Locate every blood parasite and identify its species.
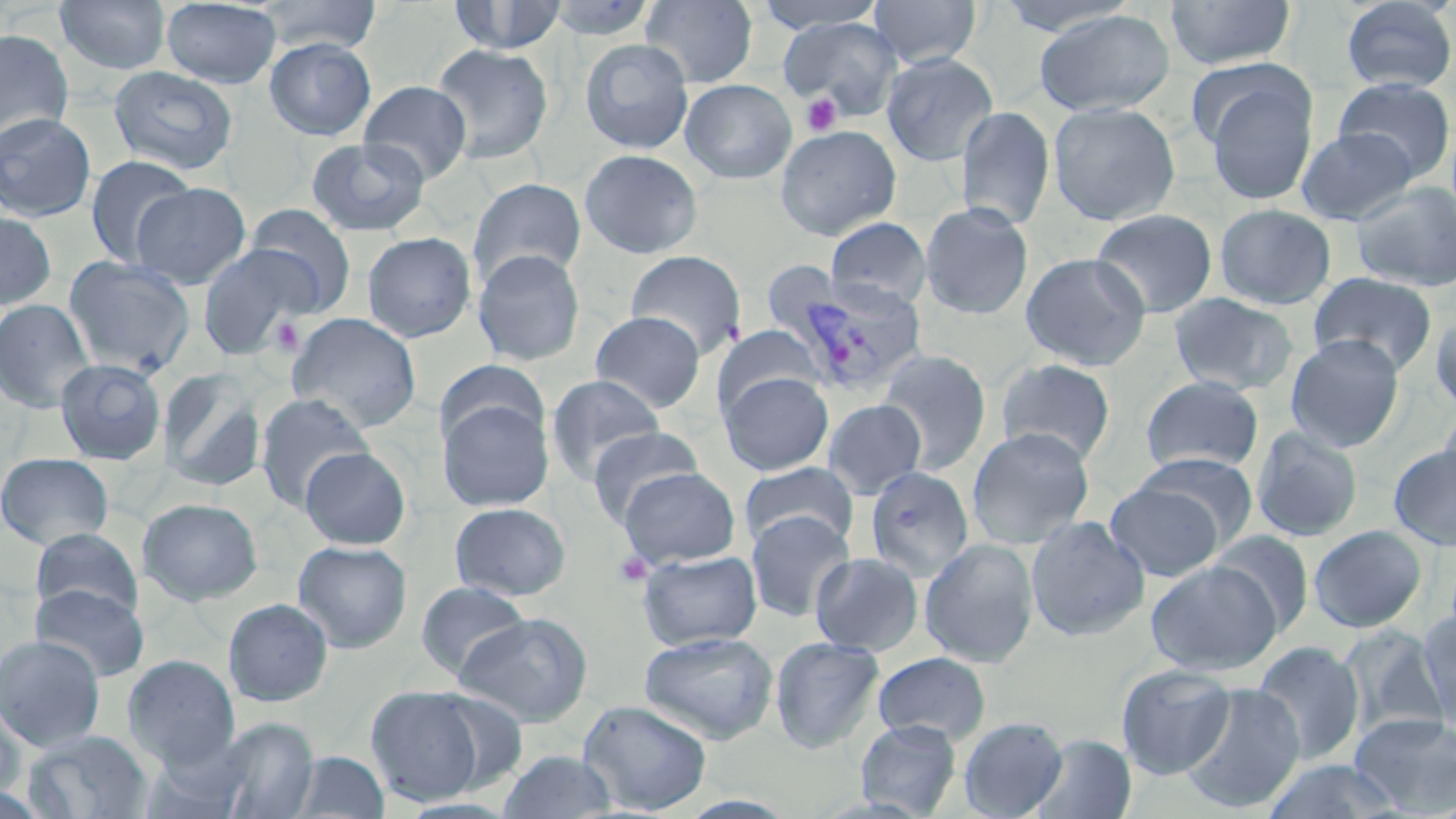
Approximate bounding boxes as (x1,y1)-(x2,y2) corner pairs in pixels.
Plasmodium vivax-infected red blood cells: (776,274)-(928,397).
No Plasmodium falciparum, Plasmodium ovale, Plasmodium malariae, Babesia divergens, or Trypanosoma brucei observed.

Platelet locations: (801,93)-(842,137), (270,316)-(305,356), (613,551)-(652,587). Uninfected red blood cell locations: (55,0)-(171,74), (161,0)-(282,88), (253,0)-(383,54), (447,0)-(570,55), (543,0)-(659,41), (640,0)-(758,88), (868,0)-(981,69), (1163,0)-(1296,70), (1339,0)-(1456,94), (753,1)-(888,33), (989,1)-(1144,37), (1033,9)-(1176,116), (778,16)-(903,118), (0,29)-(75,147), (264,37)-(377,140), (579,38)-(694,154), (430,42)-(554,164), (881,52)-(998,166), (1185,57)-(1306,152), (107,66)-(239,176), (1200,73)-(1321,206), (1332,77)-(1455,182), (680,79)-(797,184), (358,80)-(472,185), (1047,101)-(1181,226), (956,106)-(1056,230), (0,112)-(97,222), (775,125)-(902,241), (1296,126)-(1418,225), (307,137)-(430,236), (579,148)-(703,258), (85,155)-(196,269), (468,178)-(586,286), (1350,181)-(1456,291), (130,182)-(251,288), (919,201)-(1034,320), (1214,203)-(1336,310), (243,204)-(356,316), (1090,208)-(1218,318), (0,210)-(58,309), (825,218)-(932,310), (361,232)-(477,342), (198,245)-(312,360), (472,248)-(586,366), (624,250)-(747,359), (1020,252)-(1151,371), (63,255)-(195,377), (1308,272)-(1437,376), (1168,292)-(1299,396), (0,299)-(97,413), (1430,309)-(1456,415), (590,310)-(706,412), (287,312)-(422,432), (713,325)-(825,417), (1285,334)-(1405,452), (876,349)-(992,474), (995,357)-(1116,465), (54,358)-(166,465), (435,360)-(549,452), (159,369)-(267,492), (719,371)-(834,475), (545,373)-(666,486), (1139,375)-(1264,475), (255,393)-(374,512), (437,395)-(554,512), (822,399)-(927,499), (1438,405)-(1456,503), (586,425)-(704,527), (966,425)-(1096,548), (1252,426)-(1363,542), (1388,443)-(1456,551), (298,446)-(411,550), (1133,451)-(1259,544), (0,452)-(114,550), (739,461)-(858,550), (864,466)-(975,582), (619,467)-(740,568), (1106,482)-(1222,581), (138,497)-(263,605), (449,502)-(571,601), (745,511)-(855,622), (1025,515)-(1150,642), (1308,524)-(1428,633), (31,528)-(143,620), (1208,530)-(1317,637), (919,539)-(1040,668), (292,540)-(412,653), (637,549)-(762,650), (810,552)-(924,656), (1147,561)-(1282,675), (414,581)-(533,680), (30,583)-(149,682), (222,598)-(334,707), (1417,608)-(1456,730), (454,612)-(593,726), (1337,624)-(1449,741), (638,631)-(779,744), (0,634)-(106,751), (769,636)-(885,754), (1251,640)-(1366,764), (873,651)-(991,744), (123,654)-(240,770), (1116,663)-(1236,779), (1178,682)-(1305,815), (365,685)-(488,807), (577,699)-(713,815), (0,704)-(26,802), (1349,712)-(1456,814), (212,716)-(319,818), (958,716)-(1067,818), (855,718)-(962,817), (23,730)-(153,819), (1028,733)-(1137,819), (497,749)-(619,818), (288,751)-(390,818), (1262,759)-(1408,818). Slide-level diagnosis: Plasmodium vivax. Thin blood film. May-Grünwald-Giemsa stain. Captured at 1000x magnification. Image is 1456×819 pixels. Single field of view. Optical microscopy.